Identify the parasite.
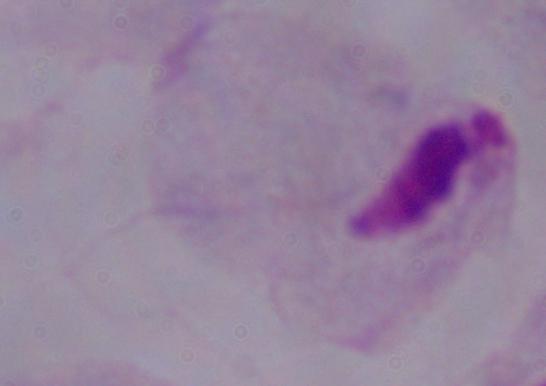

This is a trichomonad.

Summary:
  - Magnification: 1000x
  - Modality: photomicrograph